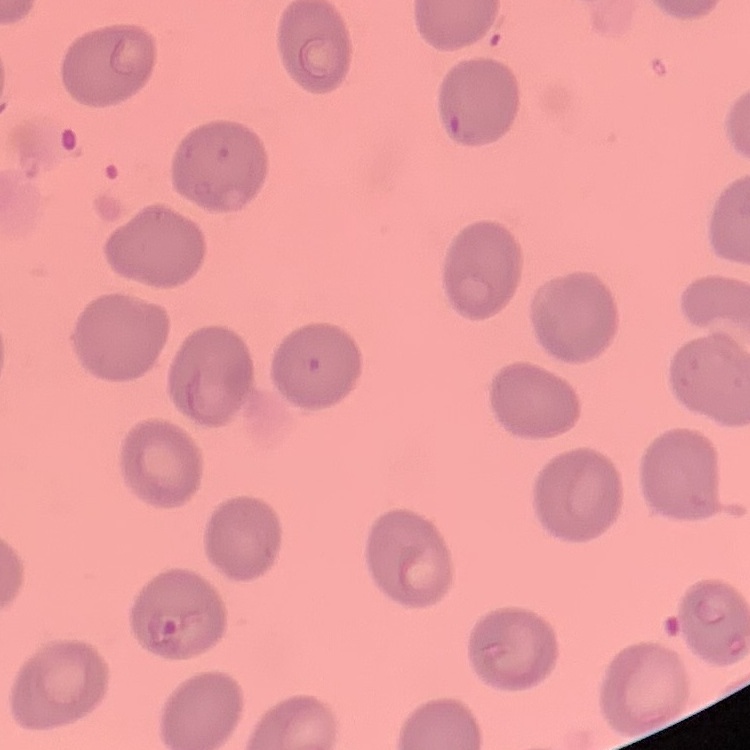 The erythrocytes exhibit no rouleaux formation. Field's or Giemsa stain. One tile cut from a larger photomicrograph. Thin blood smear.